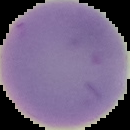

preparation = thin blood smear
result = no malaria parasites detected
image size = 130×130 pixels
image type = cell region segmented out of the field of view; surrounding area masked to black